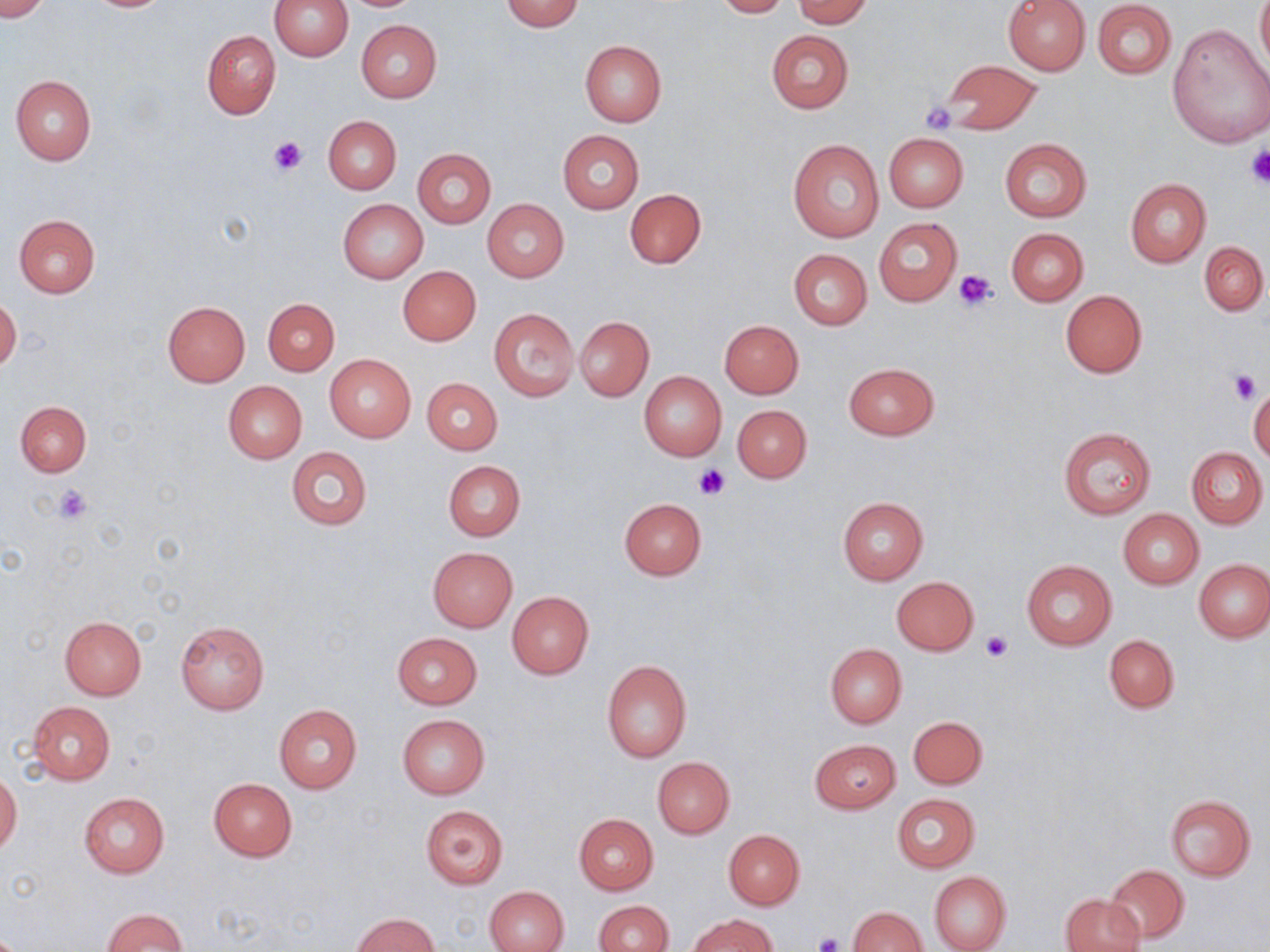

slide-level diagnosis = no evidence of blood parasites
uninfected red blood cell locations = approximate bounding boxes as named x1/y1/x2/y2 corners in pixels: (x1=0, y1=0, x2=52, y2=20), (x1=269, y1=0, x2=353, y2=60), (x1=499, y1=0, x2=584, y2=31), (x1=712, y1=0, x2=791, y2=17), (x1=792, y1=0, x2=872, y2=27), (x1=1003, y1=0, x2=1090, y2=75), (x1=1256, y1=0, x2=1269, y2=73), (x1=1092, y1=1, x2=1176, y2=79), (x1=357, y1=19, x2=442, y2=103), (x1=1166, y1=22, x2=1269, y2=150), (x1=202, y1=30, x2=281, y2=119), (x1=766, y1=30, x2=854, y2=115), (x1=579, y1=40, x2=666, y2=128), (x1=937, y1=60, x2=1041, y2=135), (x1=10, y1=75, x2=97, y2=166), (x1=323, y1=116, x2=401, y2=193), (x1=558, y1=130, x2=644, y2=214), (x1=883, y1=132, x2=968, y2=212), (x1=999, y1=138, x2=1092, y2=221), (x1=787, y1=139, x2=884, y2=244), (x1=412, y1=148, x2=496, y2=227), (x1=1125, y1=178, x2=1212, y2=268), (x1=624, y1=188, x2=706, y2=268), (x1=337, y1=199, x2=427, y2=282), (x1=482, y1=199, x2=569, y2=282), (x1=14, y1=214, x2=101, y2=299), (x1=873, y1=216, x2=963, y2=307), (x1=1006, y1=228, x2=1088, y2=306), (x1=1200, y1=240, x2=1268, y2=316), (x1=789, y1=249, x2=872, y2=329), (x1=398, y1=266, x2=480, y2=345), (x1=1060, y1=290, x2=1146, y2=378), (x1=0, y1=295, x2=21, y2=372), (x1=263, y1=298, x2=339, y2=375), (x1=162, y1=301, x2=251, y2=387), (x1=489, y1=308, x2=579, y2=400), (x1=575, y1=315, x2=654, y2=401), (x1=720, y1=319, x2=804, y2=398), (x1=324, y1=355, x2=416, y2=443), (x1=843, y1=363, x2=939, y2=440), (x1=638, y1=371, x2=727, y2=461), (x1=422, y1=377, x2=502, y2=454), (x1=223, y1=380, x2=307, y2=463), (x1=1249, y1=384, x2=1270, y2=463), (x1=15, y1=401, x2=92, y2=476), (x1=732, y1=404, x2=811, y2=483), (x1=1058, y1=426, x2=1156, y2=518), (x1=1186, y1=446, x2=1267, y2=529), (x1=286, y1=447, x2=373, y2=530), (x1=442, y1=461, x2=525, y2=541), (x1=837, y1=496, x2=929, y2=586), (x1=619, y1=498, x2=707, y2=579), (x1=1118, y1=510, x2=1203, y2=589), (x1=428, y1=547, x2=517, y2=631), (x1=1022, y1=559, x2=1117, y2=651), (x1=1194, y1=559, x2=1270, y2=641), (x1=892, y1=576, x2=979, y2=655), (x1=507, y1=591, x2=594, y2=678), (x1=58, y1=615, x2=147, y2=700), (x1=176, y1=621, x2=269, y2=714), (x1=391, y1=632, x2=482, y2=710), (x1=1104, y1=635, x2=1179, y2=713), (x1=825, y1=643, x2=906, y2=728), (x1=602, y1=659, x2=692, y2=761), (x1=26, y1=700, x2=116, y2=784), (x1=273, y1=705, x2=362, y2=793), (x1=398, y1=714, x2=490, y2=799), (x1=909, y1=716, x2=987, y2=788), (x1=811, y1=739, x2=900, y2=814), (x1=653, y1=757, x2=735, y2=838), (x1=0, y1=771, x2=22, y2=854), (x1=208, y1=779, x2=298, y2=861), (x1=79, y1=793, x2=169, y2=879), (x1=891, y1=793, x2=979, y2=873), (x1=1165, y1=794, x2=1256, y2=880), (x1=419, y1=804, x2=508, y2=889), (x1=574, y1=814, x2=658, y2=894), (x1=723, y1=829, x2=804, y2=909), (x1=1106, y1=864, x2=1188, y2=944), (x1=929, y1=872, x2=1011, y2=952), (x1=485, y1=885, x2=569, y2=952), (x1=1061, y1=893, x2=1145, y2=952), (x1=593, y1=901, x2=672, y2=952), (x1=848, y1=906, x2=926, y2=952), (x1=102, y1=908, x2=188, y2=951), (x1=351, y1=913, x2=439, y2=951), (x1=691, y1=914, x2=776, y2=952)
modality = optical microscopy
stain = May-Grünwald-Giemsa
field of view = one of a larger specimen
magnification = 1000x
image size = 1270×952 pixels
platelet locations = approximate bounding boxes as named x1/y1/x2/y2 corners in pixels: (x1=922, y1=102, x2=959, y2=131), (x1=270, y1=136, x2=306, y2=174), (x1=1244, y1=145, x2=1270, y2=188), (x1=955, y1=270, x2=999, y2=311), (x1=1230, y1=369, x2=1262, y2=402), (x1=693, y1=463, x2=732, y2=500), (x1=53, y1=484, x2=93, y2=524), (x1=980, y1=631, x2=1012, y2=662), (x1=811, y1=932, x2=844, y2=952)
preparation = thin blood smear